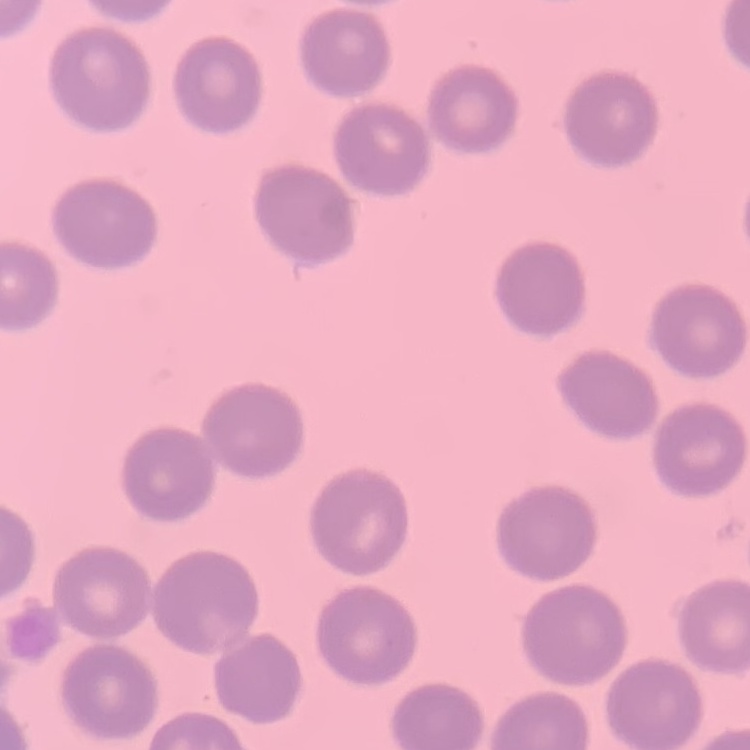
red blood cell morphology = no rouleaux formation
preparation = thin blood film
stain = Field's or Giemsa
image type = one tile cut from a larger photomicrograph